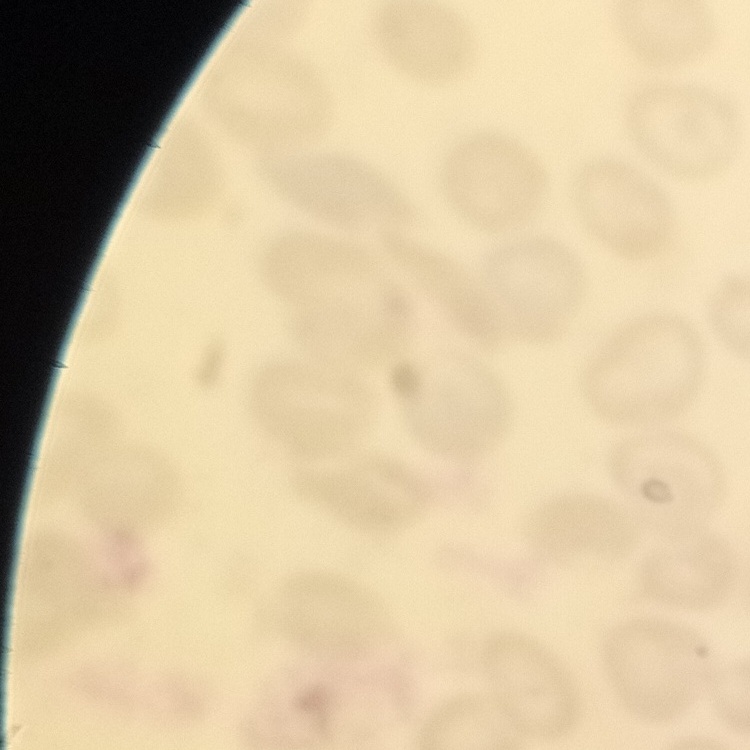
Summary:
  - Red blood cell morphology: no rouleaux formation
  - Image type: square crop of a larger photomicrograph
  - Preparation: thin blood film
  - Stain: Field's or Giemsa